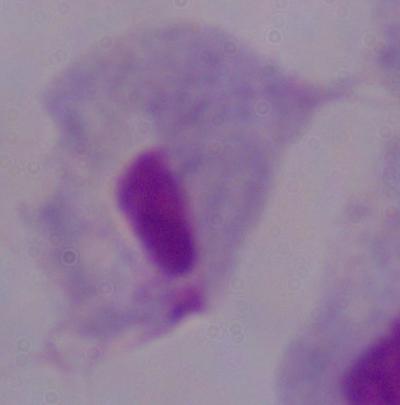
Summary:
  - Magnification: 1000x
  - Identification: trichomonad
  - Modality: micrograph